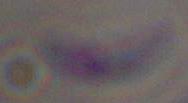

Captured at 1000x magnification. Micrograph. Toxoplasma gondii is seen.